State the blood parasite species.
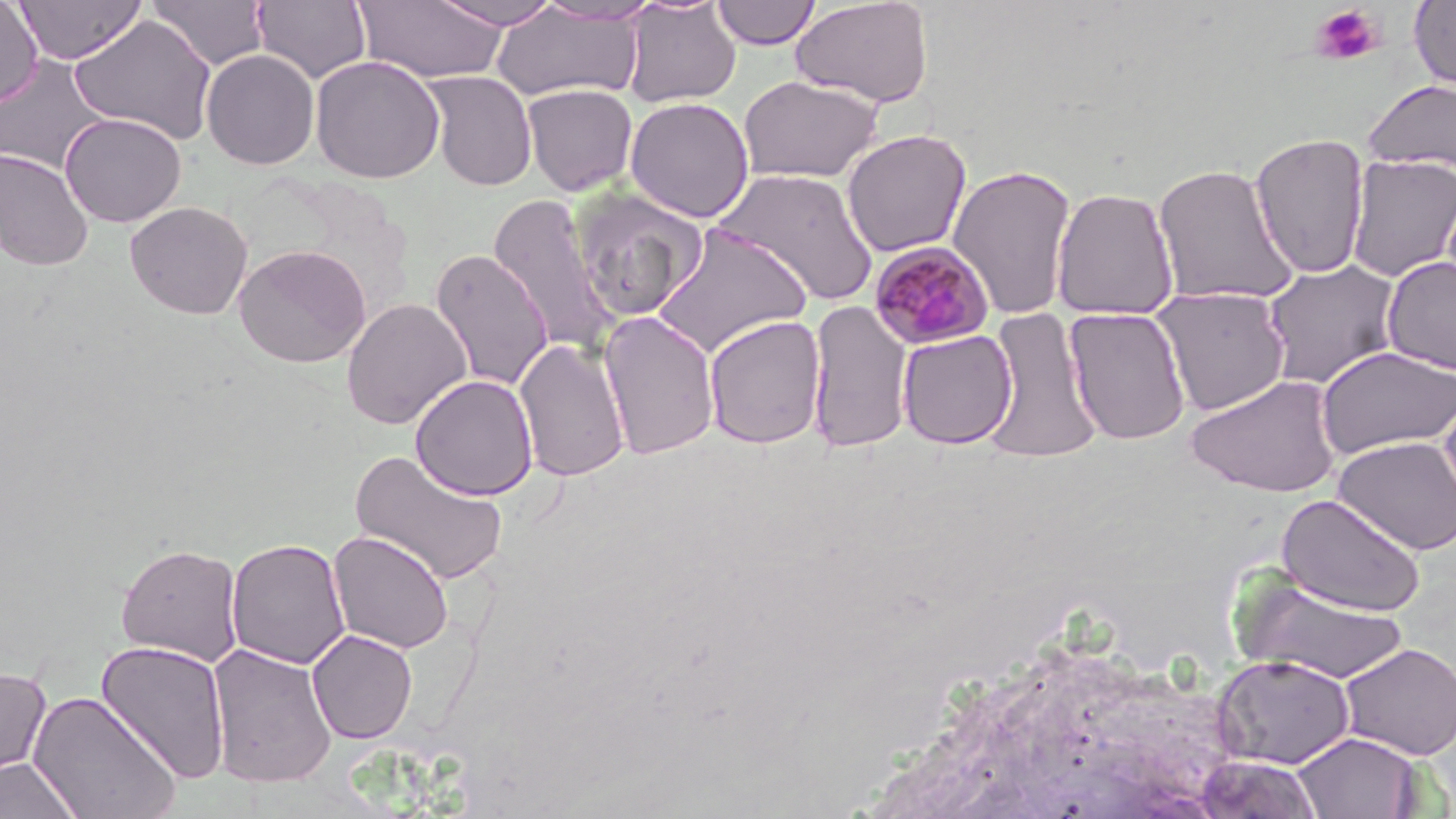

Plasmodium malariae.

Approximate bounding boxes as (x1, y1, x2, y2) in pixels. Uninfected red blood cell locations: (14, 0, 147, 64), (428, 0, 567, 29), (711, 0, 822, 50), (1409, 0, 1456, 92), (0, 1, 43, 108), (147, 1, 270, 70), (252, 1, 372, 84), (353, 1, 509, 84), (621, 1, 741, 108), (790, 1, 935, 108), (489, 5, 644, 103), (68, 14, 217, 144), (201, 49, 320, 170), (0, 54, 111, 175), (310, 55, 446, 184), (422, 70, 538, 191), (738, 74, 884, 183), (1363, 79, 1456, 174), (521, 83, 639, 196), (624, 97, 755, 223), (59, 112, 187, 227), (841, 129, 972, 257), (1249, 131, 1371, 279), (0, 149, 94, 271), (1345, 153, 1456, 282), (1152, 162, 1299, 307), (947, 163, 1078, 320), (711, 168, 880, 308), (568, 186, 708, 322), (1050, 186, 1180, 320), (487, 192, 621, 359), (125, 201, 253, 319), (651, 224, 813, 359), (233, 244, 371, 368), (430, 249, 553, 392), (1382, 256, 1456, 375), (1261, 258, 1403, 389), (1150, 286, 1291, 416), (341, 298, 472, 430), (805, 299, 915, 454), (982, 306, 1102, 464), (1063, 306, 1192, 446), (597, 310, 721, 461), (702, 314, 827, 450), (897, 329, 1018, 450), (513, 338, 631, 482), (1316, 345, 1456, 460), (1185, 373, 1343, 498), (410, 374, 538, 501), (1438, 382, 1456, 522), (1333, 436, 1456, 555), (349, 448, 510, 586), (1276, 492, 1426, 617), (328, 531, 455, 654), (226, 538, 351, 670), (114, 542, 244, 666), (1232, 572, 1410, 684), (307, 629, 418, 744), (95, 639, 232, 785), (1338, 642, 1456, 760), (206, 643, 338, 788), (1212, 654, 1356, 769), (0, 666, 52, 787), (28, 690, 182, 819), (1292, 731, 1425, 818), (1200, 753, 1325, 815), (0, 757, 82, 819). Platelet locations: (1310, 5, 1384, 66). Plasmodium malariae-infected red blood cell locations: (868, 241, 995, 350). May-Grünwald-Giemsa-stained preparation. Image is 1456×819 pixels. Single field of view. Captured at 1000x magnification. Thin blood smear. Light microscopy.